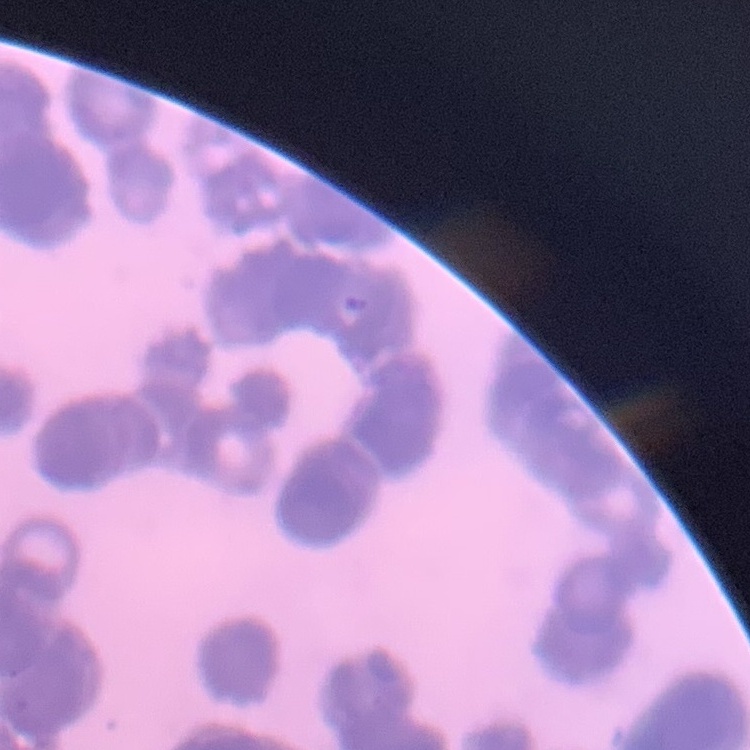

The red blood cells exhibit rouleaux formation. Thin peripheral smear. Field's or Giemsa stain. One tile cut from a larger photomicrograph.